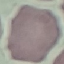
Summary:
  - Malaria status: uninfected
  - Preparation: thin blood smear
  - Stain: Giemsa
  - Capture: smartphone through the microscope eyepiece
  - Image type: cell patch, automatically extracted from a larger field of view and resized to 64 × 64 pixels